Locate every Plasmodium parasite.
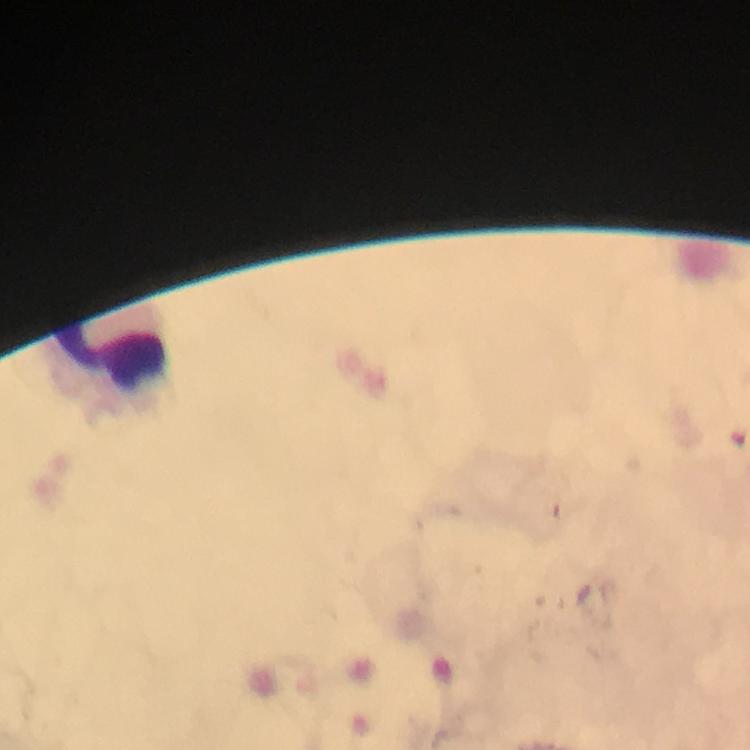

No Plasmodium parasites seen.

capture = smartphone mounted on the microscope
context = from a diagnostic examination for malaria
image size = 750×750 pixels
cropped from = one field of view
immersion oil = used
preparation = thick blood smear
stain = Giemsa
magnification = 100x
leukocyte locations = approximate centers as (x, y) in pixels: (112, 361)